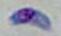
Captured at 1000x magnification. Toxoplasma gondii is shown. Micrograph.